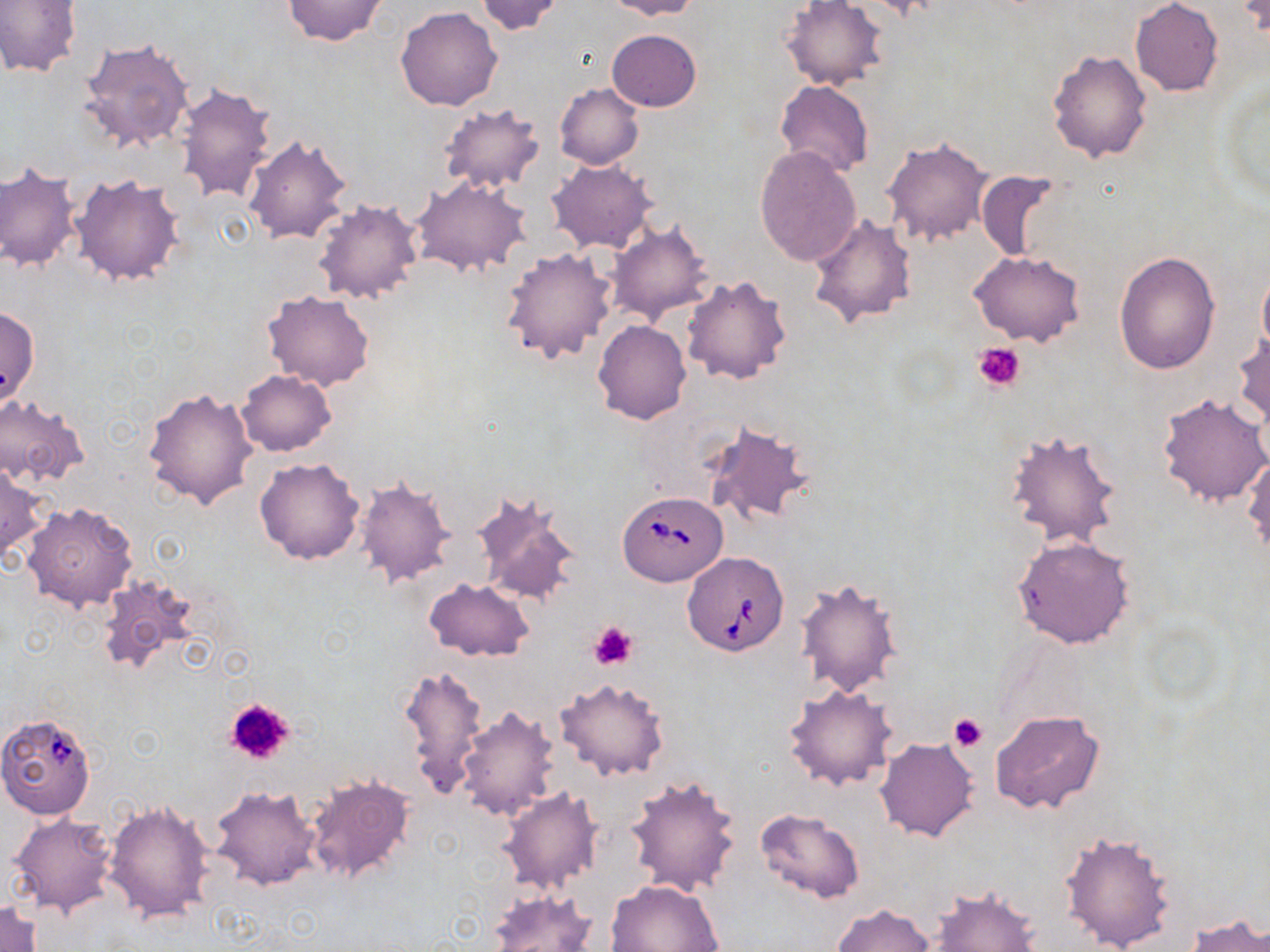

slide-level diagnosis = Babesia divergens
platelet locations = approximate bounding boxes as (x1, y1, x2, y2) in pixels: (974, 341, 1026, 391), (588, 621, 638, 671), (222, 697, 297, 767), (949, 713, 988, 752)
preparation = thin blood smear
uninfected red blood cell locations = approximate bounding boxes as (x1, y1, x2, y2) in pixels: (0, 0, 81, 77), (282, 0, 387, 46), (475, 0, 567, 37), (608, 0, 702, 20), (867, 0, 947, 23), (1240, 0, 1268, 39), (781, 1, 889, 90), (1130, 1, 1223, 96), (395, 6, 503, 111), (607, 30, 701, 112), (78, 37, 195, 154), (1047, 48, 1152, 162), (1219, 77, 1270, 200), (777, 81, 873, 178), (174, 82, 278, 205), (555, 83, 644, 168), (437, 103, 546, 194), (242, 132, 351, 242), (883, 137, 992, 245), (755, 146, 862, 267), (547, 159, 658, 254), (1, 164, 81, 273), (974, 170, 1065, 261), (71, 173, 185, 286), (410, 176, 530, 279), (312, 198, 423, 304), (807, 213, 918, 328), (607, 222, 715, 324), (499, 246, 616, 364), (968, 249, 1085, 346), (1113, 251, 1220, 374), (1257, 266, 1270, 361), (682, 274, 792, 385), (264, 291, 374, 391), (1, 305, 39, 409), (592, 320, 692, 425), (1232, 329, 1269, 430), (234, 370, 335, 456), (143, 387, 257, 510), (1157, 393, 1270, 508), (0, 396, 88, 486), (703, 419, 817, 530), (1003, 429, 1124, 550), (1244, 451, 1270, 559), (254, 458, 366, 565), (0, 463, 45, 566), (354, 475, 456, 589), (468, 489, 581, 606), (22, 501, 138, 612), (1010, 534, 1138, 650), (94, 574, 200, 679), (794, 577, 905, 698), (424, 578, 534, 662), (398, 663, 488, 802), (554, 678, 670, 782), (785, 682, 898, 792), (456, 706, 561, 822), (992, 709, 1105, 814), (875, 737, 980, 842), (303, 773, 416, 886), (625, 775, 741, 896), (208, 783, 321, 890), (499, 786, 603, 892), (105, 800, 215, 925), (754, 808, 865, 903), (7, 812, 119, 918), (1057, 830, 1177, 952), (605, 880, 723, 952), (929, 886, 1043, 952), (487, 890, 598, 952), (1, 898, 44, 952), (834, 903, 936, 951), (1185, 915, 1270, 951)
modality = optical microscopy
image size = 1270×952 pixels
field of view = one of a larger specimen
magnification = 1000x
stain = May-Grünwald-Giemsa
Babesia divergens-infected red blood cell locations = approximate bounding boxes as (x1, y1, x2, y2) in pixels: (618, 490, 728, 586), (681, 551, 791, 657), (0, 712, 97, 818)